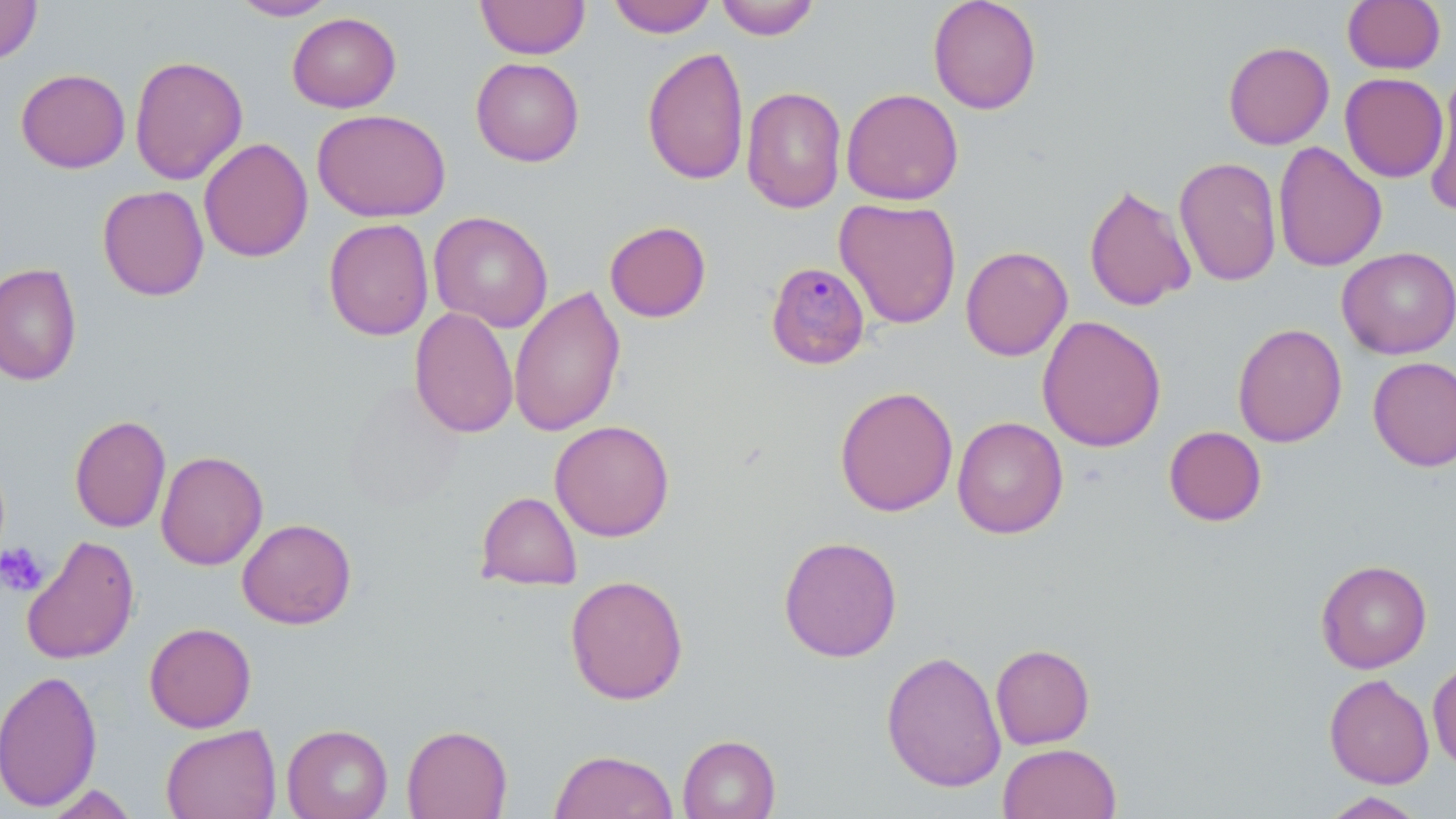

slide_level_diagnosis: Plasmodium malariae
stain: May-Grünwald-Giemsa
field_of_view: single
modality: optical microscopy
magnification: 1000x
platelet_locations: 'approximate bounding boxes as (x1,y1)-(x2,y2) corner pairs in pixels: (1,541)-(49,598)'
image_size: 1456×819 pixels
preparation: thin blood smear
plasmodium_malariae_infected_red_blood_cell_locations: 'approximate bounding boxes as (x1,y1)-(x2,y2) corner pairs in pixels: (766,261)-(871,371)'
uninfected_red_blood_cell_locations: 'approximate bounding boxes as (x1,y1)-(x2,y2) corner pairs in pixels: (0,0)-(42,66), (230,0)-(337,21), (476,0)-(590,59), (607,0)-(717,38), (715,0)-(820,40), (928,0)-(1042,115), (1342,0)-(1445,74), (287,12)-(401,112), (1223,41)-(1335,150), (642,46)-(749,186), (129,55)-(248,185), (470,57)-(584,167), (15,68)-(131,173), (1339,73)-(1449,182), (1423,80)-(1456,215), (741,86)-(847,214), (841,88)-(964,206), (312,109)-(451,223), (199,137)-(313,263), (1272,141)-(1387,272), (1173,156)-(1282,287), (1083,183)-(1197,312), (97,184)-(209,301), (834,197)-(962,330), (429,211)-(553,333), (323,218)-(434,341), (604,220)-(711,323), (960,245)-(1073,361), (1336,247)-(1456,359), (0,261)-(82,386), (509,284)-(626,437), (409,307)-(519,439), (1037,315)-(1167,452), (1232,322)-(1347,447), (1368,356)-(1456,471), (343,383)-(467,512), (834,386)-(959,517), (69,414)-(171,533), (951,416)-(1069,539), (549,420)-(675,541), (1163,426)-(1267,526), (155,450)-(268,570), (475,491)-(582,591), (236,518)-(357,629), (20,535)-(140,665), (778,535)-(903,662), (1316,559)-(1432,673), (565,574)-(689,705), (144,622)-(256,732), (990,643)-(1095,749), (880,649)-(1006,794), (1427,658)-(1456,772), (0,668)-(102,812), (1324,673)-(1434,788), (160,723)-(282,819), (281,723)-(393,819), (402,724)-(512,818), (677,734)-(781,819), (998,742)-(1121,819), (549,749)-(678,819), (42,783)-(140,818), (1320,791)-(1427,819)'